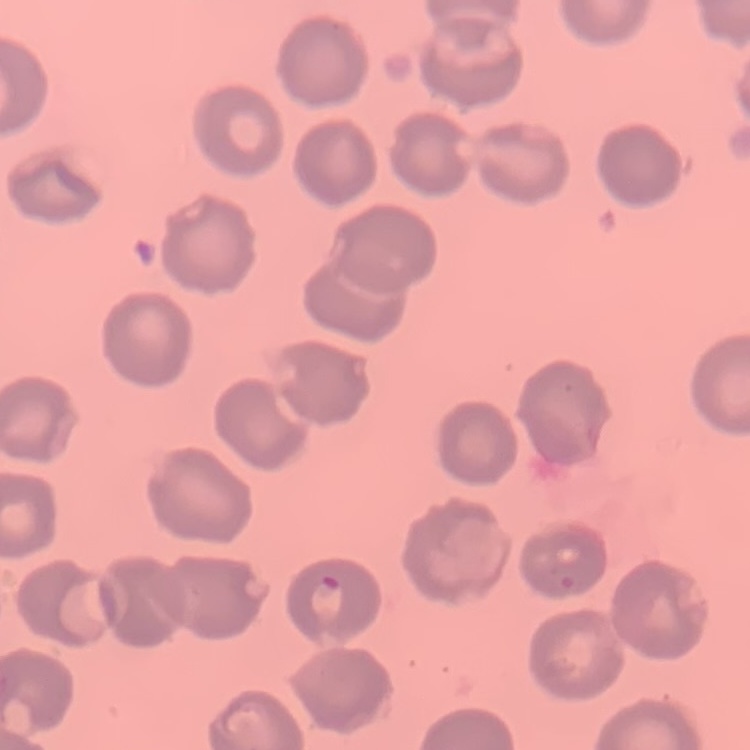

{
  "red_blood_cell_morphology": "no rouleaux formation",
  "image_type": "one tile cut from a larger photomicrograph",
  "preparation": "thin blood smear",
  "stain": "Field's or Giemsa"
}